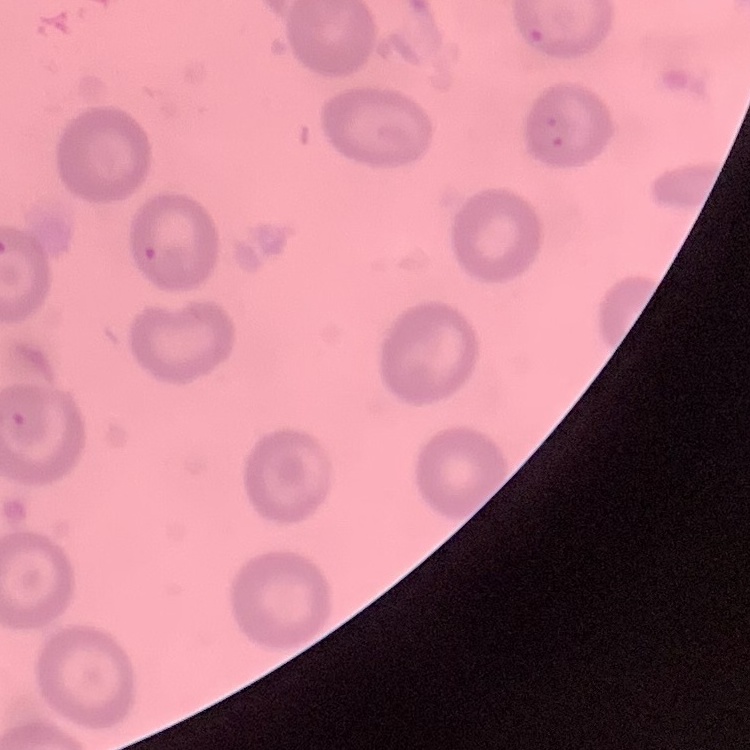

erythrocyte morphology = no rouleaux formation
image type = square crop of a larger photomicrograph
stain = Field's or Giemsa
preparation = thin peripheral smear